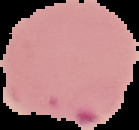

Cell region segmented out of the field of view; the surrounding area is masked to black. Image is 139×130 pixels. Result: Plasmodium parasites detected. From a thin blood film.